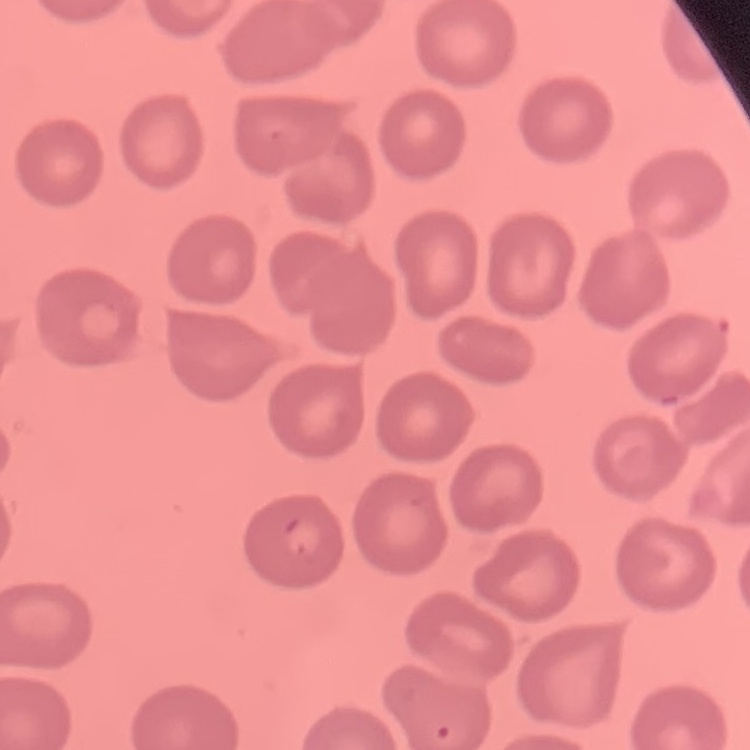
The erythrocytes show no rouleaux formation. Field's or Giemsa stain. Square crop of a larger photomicrograph. Thin peripheral smear.